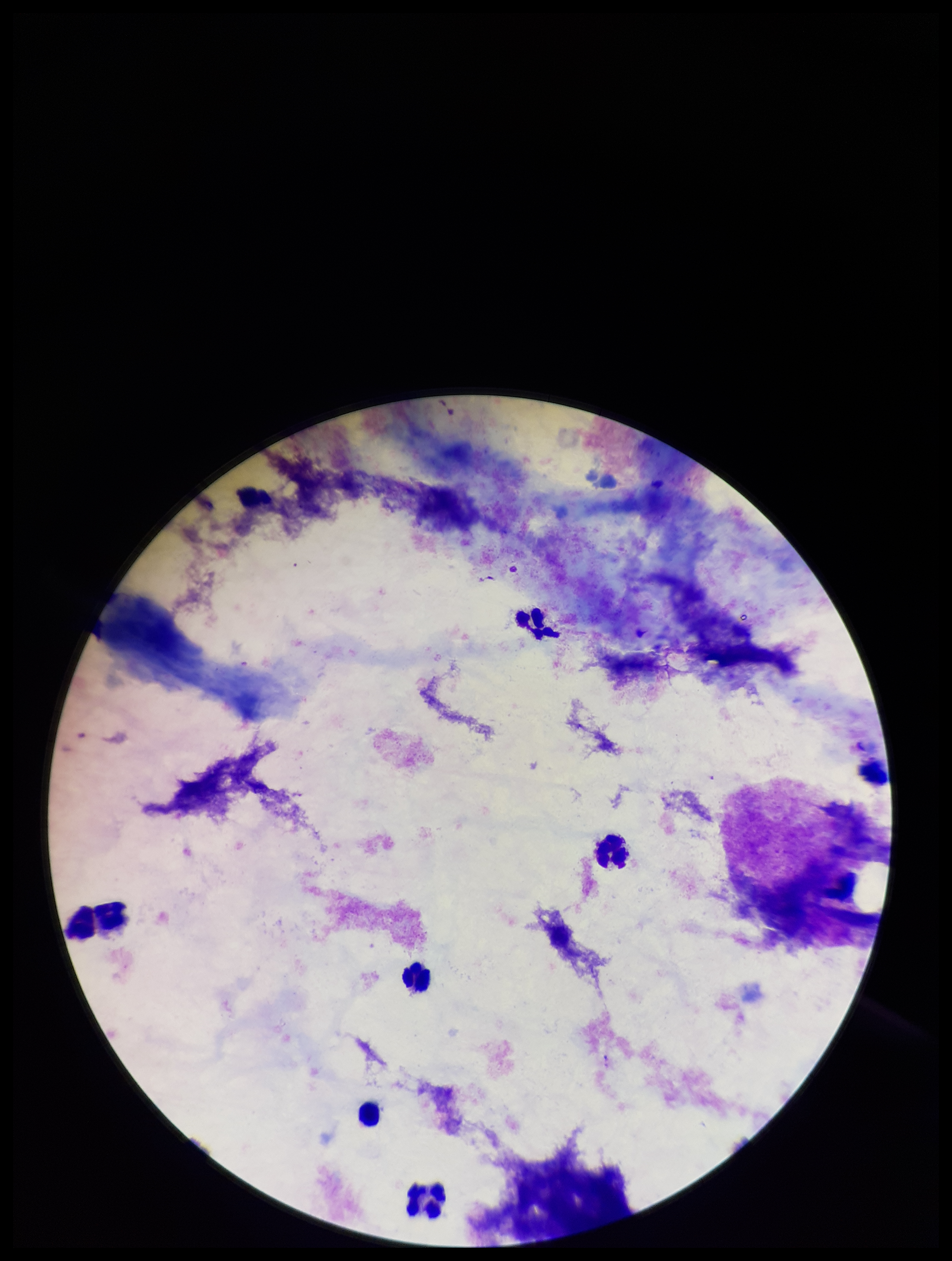
Summary:
  - Preparation: thick blood smear
  - Field of view: one from this slide
  - Plasmodium parasites: none identified
  - Image size: 952×1261 pixels
  - Stain: Giemsa
  - Capture: smartphone photograph through the microscope eyepiece
  - Leukocyte count: 5
  - Parasite count: 0
  - Patient malaria status: negative